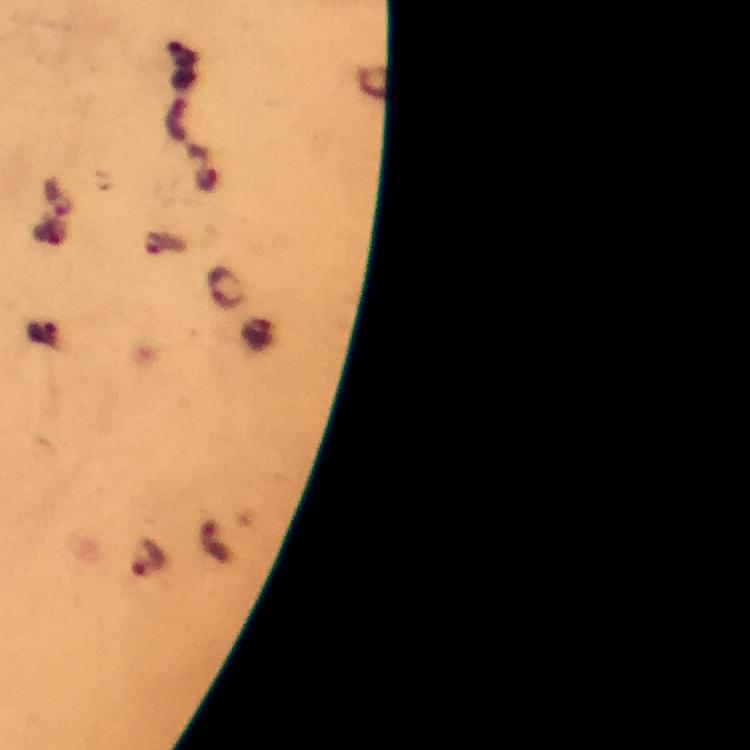

Approximate centers as (x, y) in pixels.
Summary:
  - Malaria parasite locations: (60, 196), (149, 558)
  - Magnification: 100x
  - Cropped from: one field of view
  - Capture: smartphone camera through the microscope
  - Image size: 750×750 pixels
  - Context: from a malaria diagnostic workup
  - Immersion oil: used
  - Preparation: thick blood smear
  - Stain: Giemsa